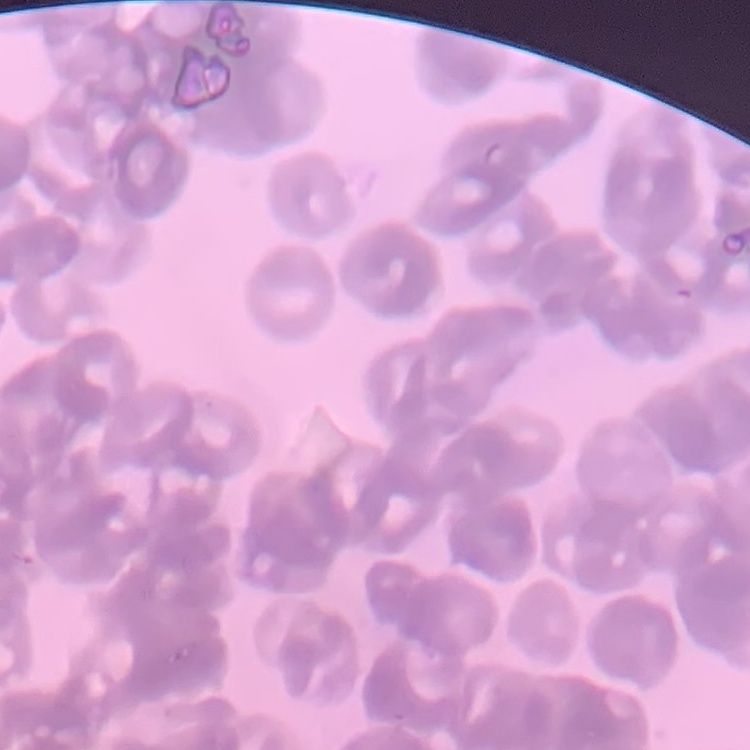

erythrocyte morphology = rouleaux formation
image type = one tile cut from a larger photomicrograph
stain = Field's or Giemsa
preparation = thin peripheral smear